Locate every Plasmodium parasite.
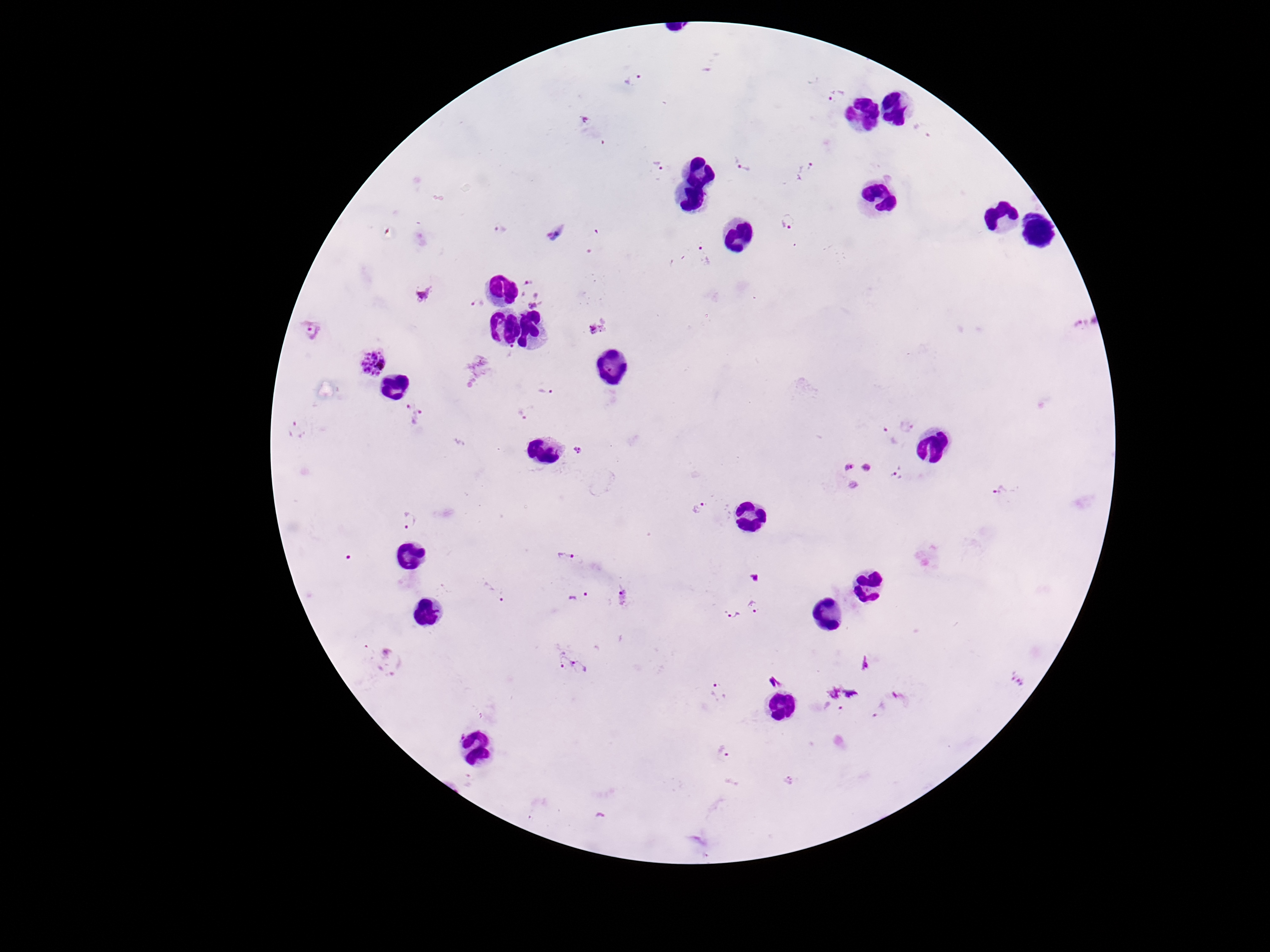
Approximate centers as (x, y) in pixels.
Plasmodium parasites: (633, 78), (836, 95), (585, 121), (924, 133), (744, 164), (658, 166), (803, 169), (789, 221), (500, 230), (556, 234), (705, 255), (531, 292), (426, 295), (478, 304), (1090, 325), (311, 329), (514, 349), (373, 362), (545, 390), (412, 414), (524, 414), (911, 427), (298, 431), (888, 436), (577, 452), (859, 473), (899, 476), (1001, 491), (699, 509), (409, 520), (566, 556), (495, 590), (580, 596), (621, 598), (759, 608), (731, 615), (388, 662), (572, 664), (1019, 680), (719, 692), (725, 752), (789, 780), (470, 781), (600, 816).

Summary:
  - Image size: 1270×952 pixels
  - Stain: Giemsa
  - Magnification: 100x
  - Field of view: single
  - Capture: smartphone camera through the microscope eyepiece
  - Preparation: thick peripheral-blood smear
  - Patient malaria status: positive